Report the malaria status of this cell.
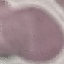

It is uninfected.

Summary:
  - Preparation: thin smear
  - Image type: automatically extracted cell patch, resized to 64 × 64 pixels
  - Capture: smartphone through the microscope eyepiece
  - Stain: Giemsa